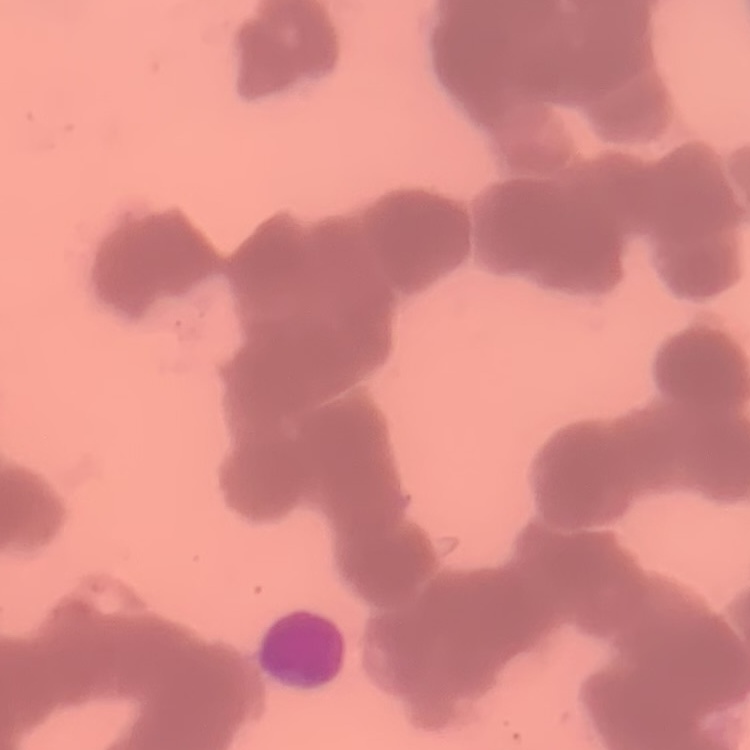
erythrocyte morphology = rouleaux formation
stain = Field's or Giemsa
preparation = thin blood film
image type = square crop of a larger photomicrograph